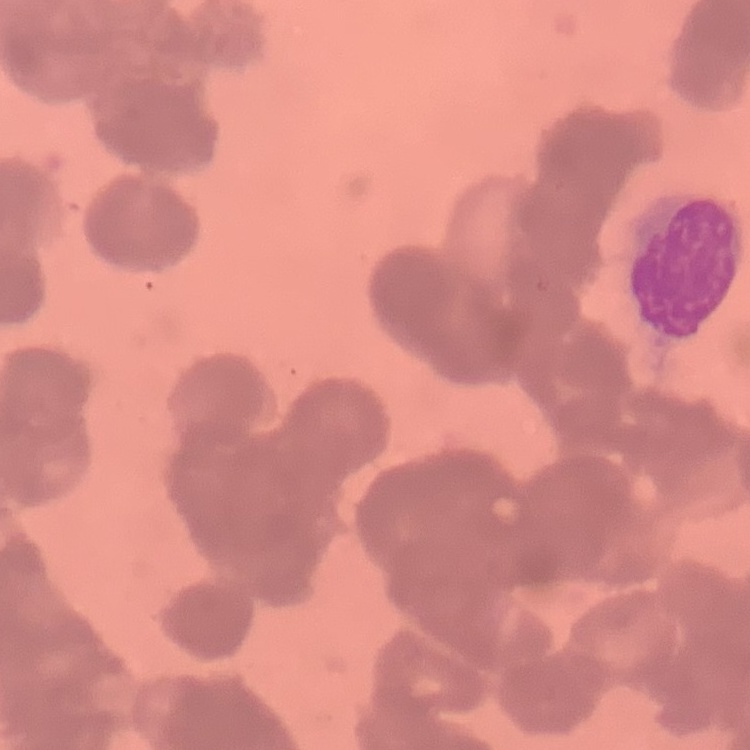
The red blood cells show rouleaux formation. Field's or Giemsa stain. Square crop of a larger photomicrograph. Thin blood film.